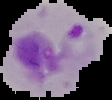

Summary:
  - Image size: 112×100 pixels
  - Preparation: thin blood smear
  - Result: Plasmodium parasites detected
  - Image type: cell region segmented out of the field of view; surrounding area masked to black